Give the extent of all Plasmodium falciparum-infected red blood cells.
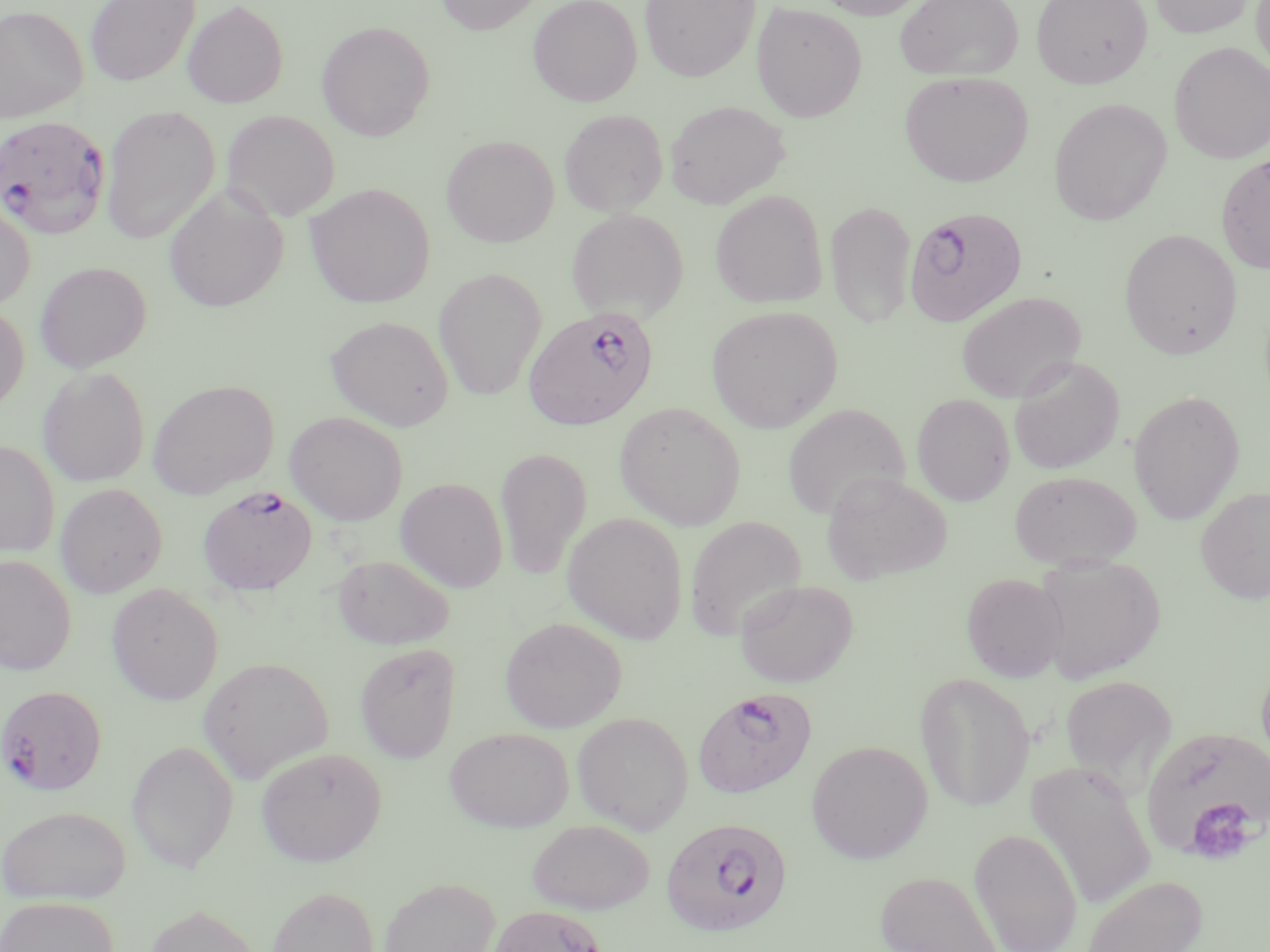
Approximate bounding boxes as (x1, y1, x2, y2) in pixels.
Plasmodium falciparum-infected red blood cells: (0, 115, 112, 240), (904, 207, 1028, 327), (523, 306, 658, 432), (198, 485, 318, 596), (0, 684, 107, 795), (693, 687, 817, 798), (661, 817, 793, 938).

Platelet locations: (1182, 798, 1261, 865). Uninfected red blood cell locations: (85, 0, 200, 87), (434, 0, 545, 35), (527, 0, 643, 106), (639, 0, 760, 82), (813, 0, 931, 20), (894, 0, 1023, 81), (1031, 0, 1153, 88), (1150, 0, 1254, 38), (1251, 0, 1270, 74), (182, 1, 289, 108), (751, 1, 868, 122), (0, 4, 88, 123), (317, 20, 435, 141), (1169, 41, 1270, 163), (899, 71, 1034, 187), (1049, 97, 1171, 226), (664, 100, 790, 209), (100, 106, 220, 244), (559, 108, 668, 216), (222, 109, 340, 222), (441, 135, 559, 247), (1215, 154, 1270, 274), (304, 183, 435, 308), (163, 185, 288, 313), (710, 190, 827, 309), (825, 199, 917, 328), (0, 201, 35, 311), (566, 207, 689, 322), (1118, 228, 1242, 360), (35, 261, 151, 373), (433, 267, 546, 401), (956, 291, 1086, 404), (0, 303, 29, 414), (706, 305, 842, 432), (326, 315, 454, 431), (1008, 356, 1125, 475), (37, 366, 150, 487), (147, 379, 279, 499), (1128, 389, 1245, 525), (912, 393, 1015, 506), (614, 402, 746, 531), (782, 403, 910, 521), (285, 411, 408, 525), (0, 440, 60, 558), (495, 446, 592, 582), (1008, 469, 1143, 570), (821, 471, 952, 585), (396, 477, 508, 593), (55, 483, 167, 597), (1196, 486, 1270, 604), (562, 512, 687, 644), (684, 515, 807, 641), (331, 553, 455, 650), (1032, 553, 1165, 683), (0, 554, 77, 676), (961, 572, 1068, 682), (735, 579, 858, 688), (105, 582, 223, 705), (499, 616, 627, 732), (354, 642, 462, 763), (198, 657, 334, 783), (1256, 658, 1270, 777), (915, 671, 1034, 812), (1058, 674, 1178, 790), (572, 711, 694, 834), (1139, 723, 1270, 866), (444, 727, 574, 832), (126, 740, 239, 873), (806, 740, 933, 864), (255, 746, 387, 866), (1026, 760, 1157, 911), (1, 805, 131, 905), (526, 819, 655, 915), (969, 828, 1083, 951), (874, 869, 1005, 952), (1080, 874, 1208, 952), (378, 876, 500, 952), (267, 885, 379, 952), (0, 896, 119, 952), (142, 903, 264, 952), (485, 903, 608, 952). Slide-level diagnosis: Plasmodium falciparum. 1000x magnification. May-Grünwald-Giemsa-stained preparation. One field of a larger specimen. Optical microscopy. Thin blood film. Image is 1270×952 pixels.